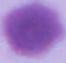 An erythrocyte is seen. Captured at 1000x magnification. Photomicrograph.